State which parasite is depicted.
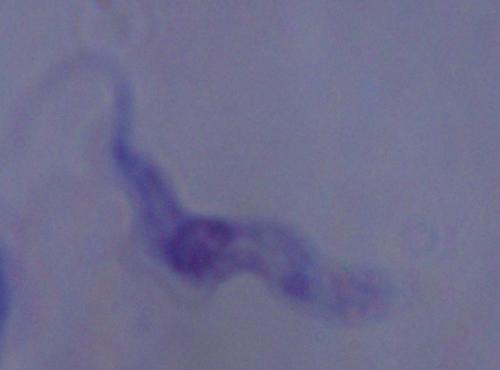

A trypanosome.

Photomicrograph. 1000x magnification.